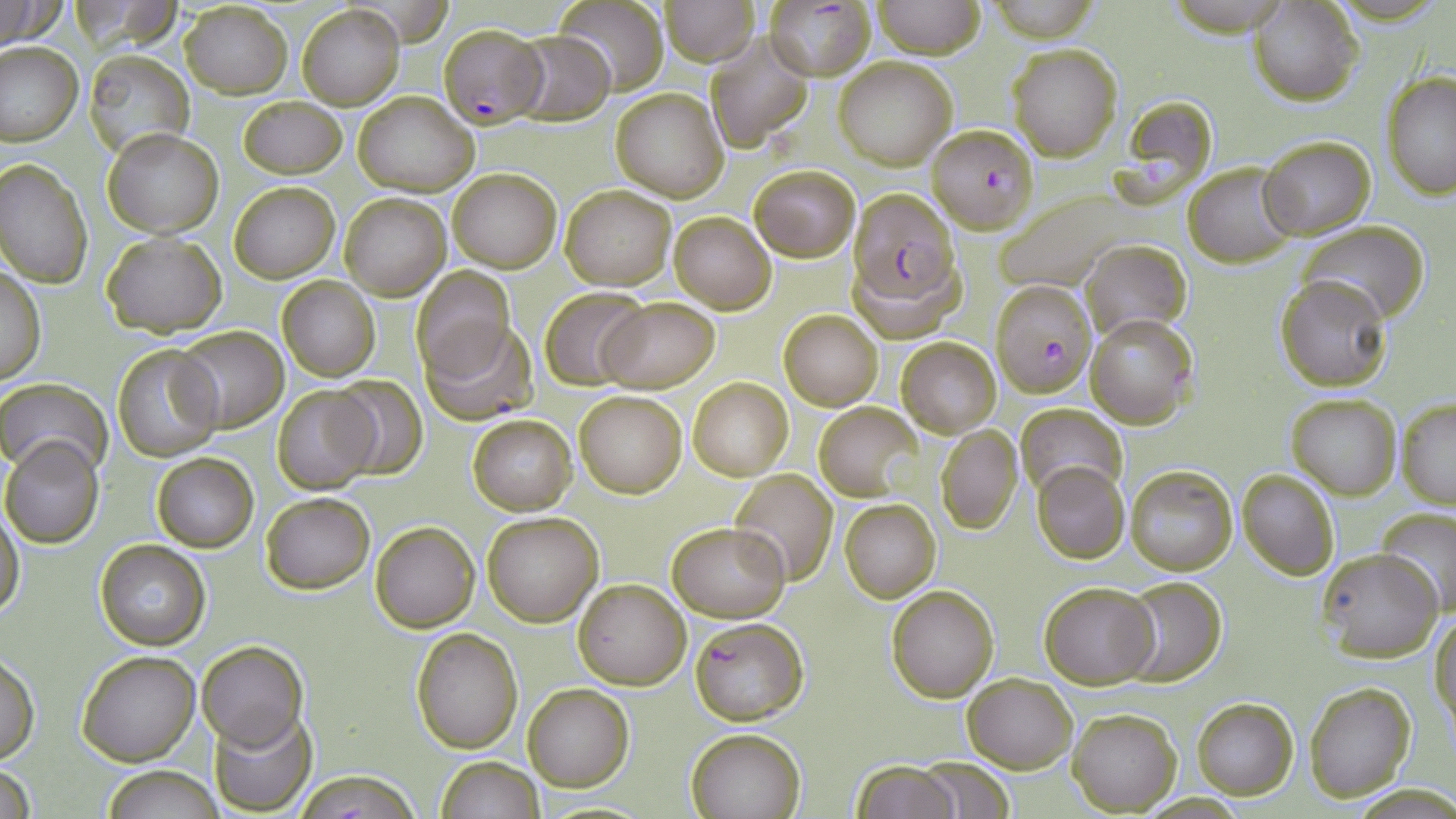
Summary:
  - Coordinate format: approximate bounding boxes as [x1, y1, x2, y2] in pixels
  - Uninfected red blood cell locations: [552, 0, 671, 95], [662, 0, 758, 65], [871, 0, 985, 59], [1, 1, 65, 49], [1247, 1, 1362, 104], [180, 3, 291, 96], [298, 4, 403, 110], [508, 30, 615, 125], [704, 33, 815, 151], [1, 41, 81, 145], [1005, 42, 1122, 161], [83, 51, 193, 155], [834, 57, 956, 170], [655, 68, 803, 189], [1382, 71, 1456, 199], [610, 88, 727, 201], [354, 92, 477, 195], [1118, 93, 1219, 200], [239, 95, 346, 179], [103, 129, 222, 237], [1261, 136, 1375, 239], [0, 159, 94, 289], [1185, 162, 1299, 268], [750, 164, 860, 261], [446, 167, 561, 272], [228, 180, 340, 283], [561, 184, 676, 290], [998, 189, 1131, 292], [340, 194, 450, 299], [668, 211, 776, 313], [1297, 221, 1430, 326], [102, 232, 227, 336], [1081, 237, 1190, 338], [847, 246, 965, 345], [1, 267, 45, 385], [410, 267, 515, 373], [1275, 274, 1394, 391], [276, 275, 381, 382], [539, 287, 650, 389], [597, 297, 721, 394], [779, 311, 883, 410], [1085, 313, 1198, 429], [421, 319, 537, 426], [174, 326, 288, 432], [897, 337, 1001, 437], [113, 345, 223, 463], [329, 374, 429, 480], [688, 377, 793, 481], [0, 378, 112, 477], [272, 386, 378, 495], [574, 391, 686, 497], [1285, 393, 1402, 497], [1395, 398, 1456, 509], [814, 403, 923, 501], [1016, 404, 1127, 499], [466, 414, 577, 514], [935, 424, 1023, 534], [1, 437, 104, 548], [150, 452, 258, 553], [1032, 462, 1129, 564], [1126, 464, 1237, 575], [1236, 468, 1339, 580], [728, 469, 839, 586], [261, 493, 374, 594], [840, 499, 940, 602], [856, 501, 967, 666], [1377, 507, 1456, 617], [0, 510, 25, 623], [481, 511, 604, 627], [371, 521, 480, 633], [666, 521, 789, 621], [96, 540, 211, 651], [1317, 548, 1442, 662], [1120, 575, 1227, 687], [572, 578, 691, 690], [1038, 579, 1159, 690], [886, 583, 999, 702], [1430, 612, 1456, 737], [411, 628, 523, 753], [197, 640, 308, 750], [76, 648, 201, 766], [1, 654, 38, 764], [962, 672, 1076, 773], [1303, 682, 1416, 802], [522, 683, 634, 790], [1191, 697, 1298, 800], [208, 706, 317, 815], [1067, 707, 1181, 815], [686, 727, 806, 818], [914, 754, 1017, 818], [435, 755, 545, 819], [850, 760, 960, 819], [1, 761, 35, 819], [99, 765, 225, 819], [294, 769, 421, 818]
  - Plasmodium falciparum-infected red blood cell locations: [766, 0, 876, 80], [442, 24, 546, 128], [926, 124, 1038, 235], [848, 188, 961, 306], [990, 279, 1095, 397], [689, 616, 810, 726]
  - Slide-level diagnosis: Plasmodium falciparum
  - Field of view: one of a larger specimen
  - Image size: 1456×819 pixels
  - Stain: May-Grünwald-Giemsa
  - Preparation: thin blood smear
  - Magnification: 1000x
  - Modality: optical microscopy